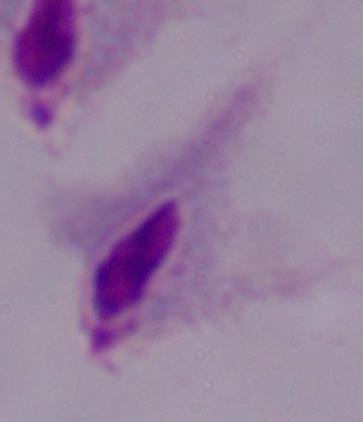

Micrograph. Captured at 1000x magnification. A trichomonad is shown.